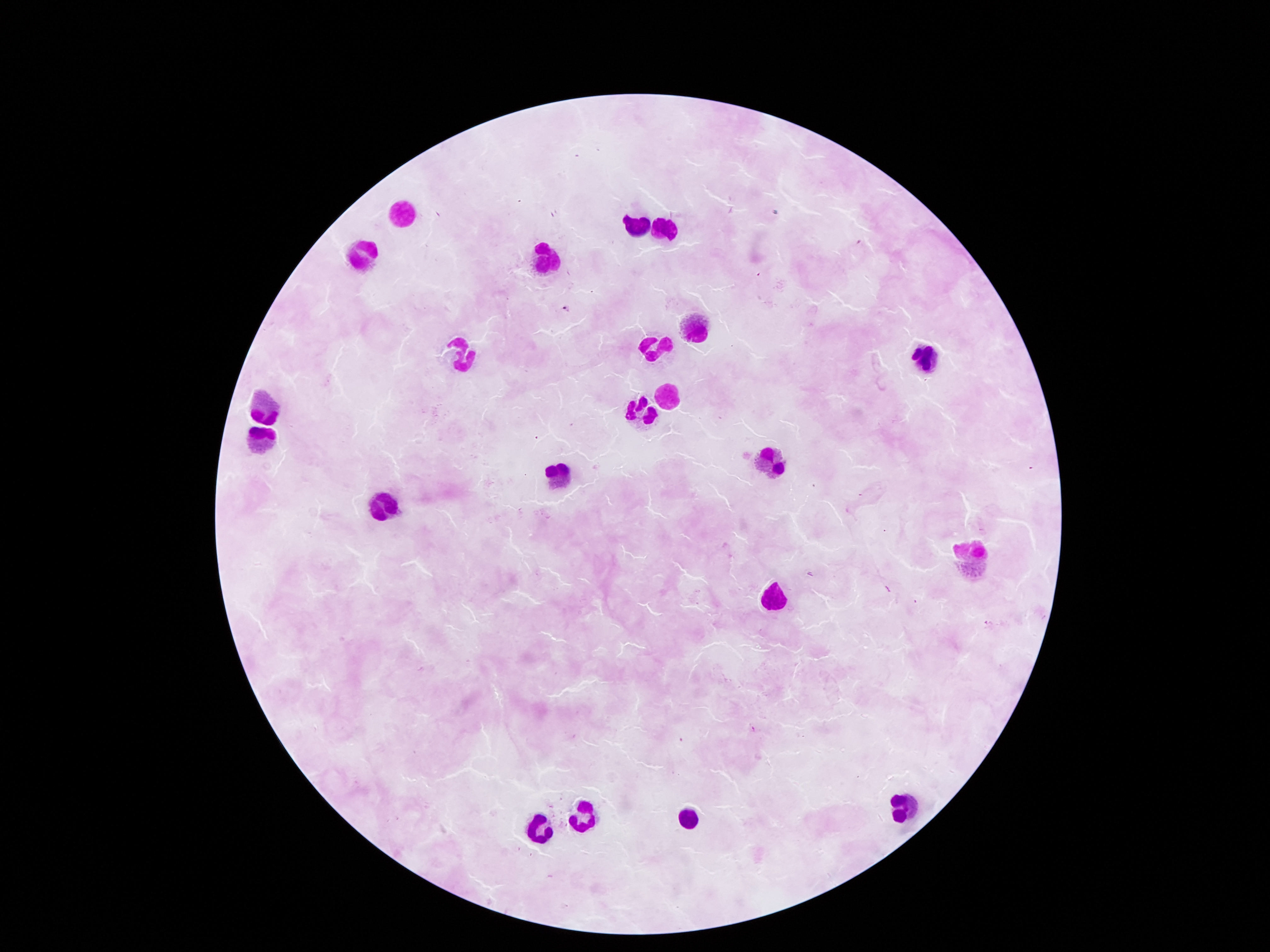 Approximate object centers, in pixels from the top-left corner. Leukocyte locations: (x=400, y=211), (x=638, y=225), (x=665, y=228), (x=363, y=256), (x=548, y=258), (x=696, y=334), (x=656, y=343), (x=461, y=353), (x=924, y=357), (x=668, y=394), (x=261, y=405), (x=642, y=411), (x=256, y=441), (x=773, y=459), (x=557, y=472), (x=380, y=509), (x=973, y=555), (x=773, y=601), (x=908, y=811), (x=583, y=818), (x=687, y=818), (x=543, y=827). Giemsa-stained preparation. Image is 1270×952 pixels. Thick peripheral-blood smear. Photographed through the microscope eyepiece with a smartphone camera. 100x magnification. Patient malaria status: uninfected. Single field of view.